Look for Plasmodium parasites.
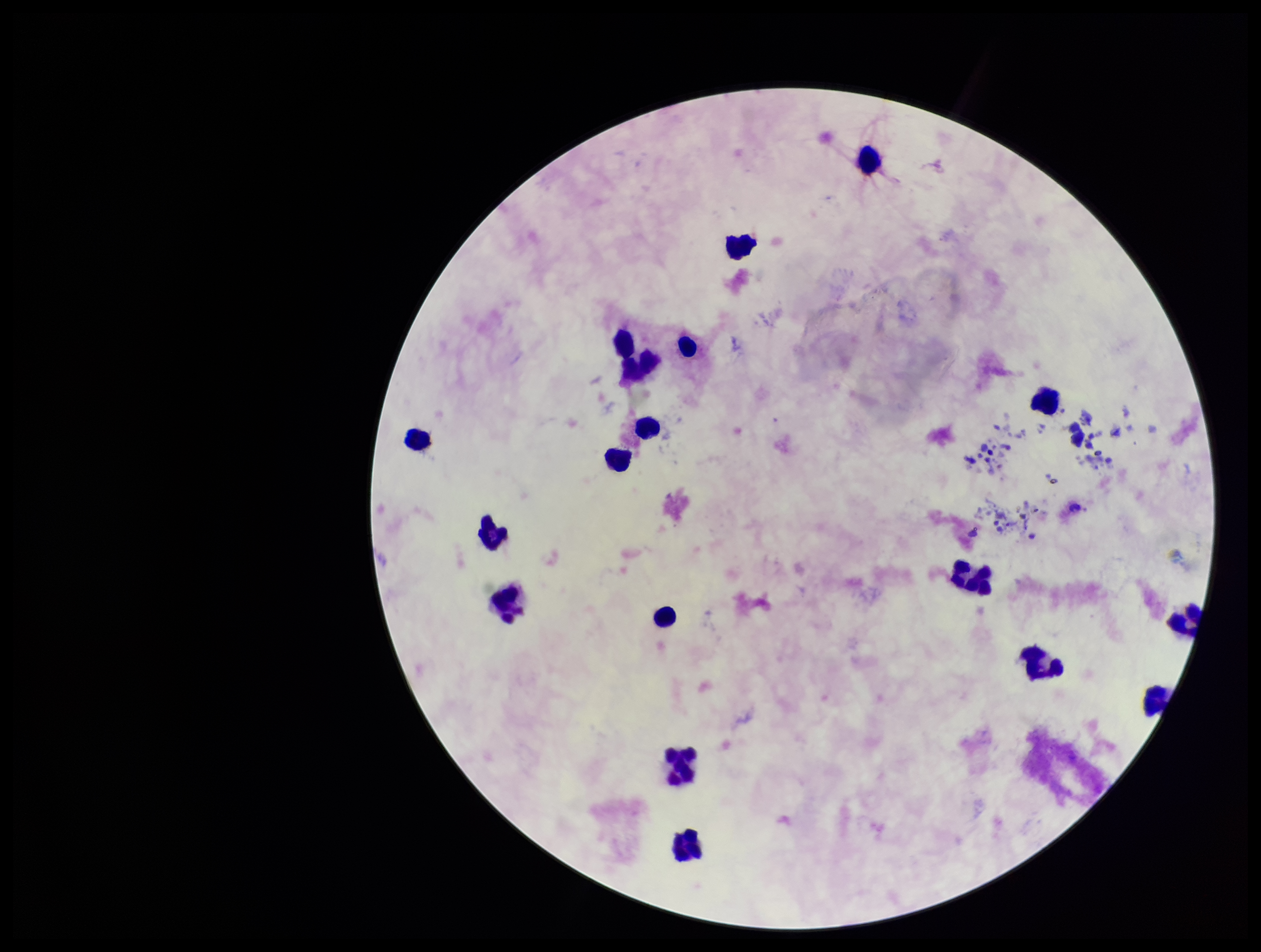

None identified.

Leukocyte count: 17. Image is 1261×952 pixels. Patient malaria status: negative. Stained with Giemsa. Smartphone photograph taken through the eyepiece of a microscope. Preparation: thick blood smear. Parasite count: 0. One field from this slide.